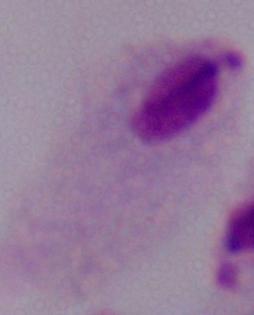

modality: photomicrograph
identification: trichomonad
magnification: 1000x